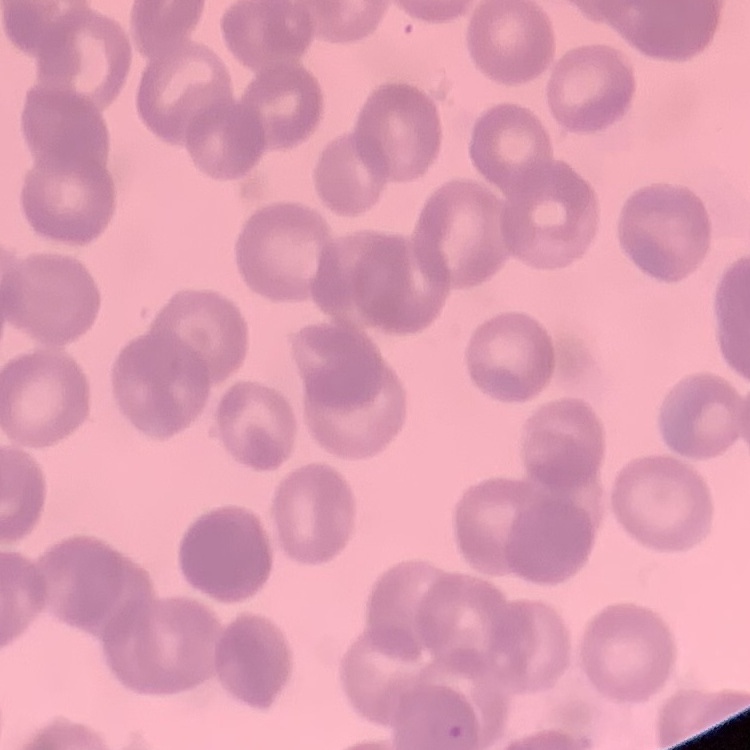

Summary:
  - Erythrocyte morphology: rouleaux formation
  - Preparation: thin peripheral smear
  - Stain: Field's or Giemsa
  - Image type: square crop of a larger photomicrograph